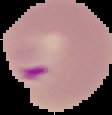
image type = cell region segmented out of the field of view; surrounding area masked to black
image size = 112×115 pixels
preparation = thin blood film
result = malaria parasites identified